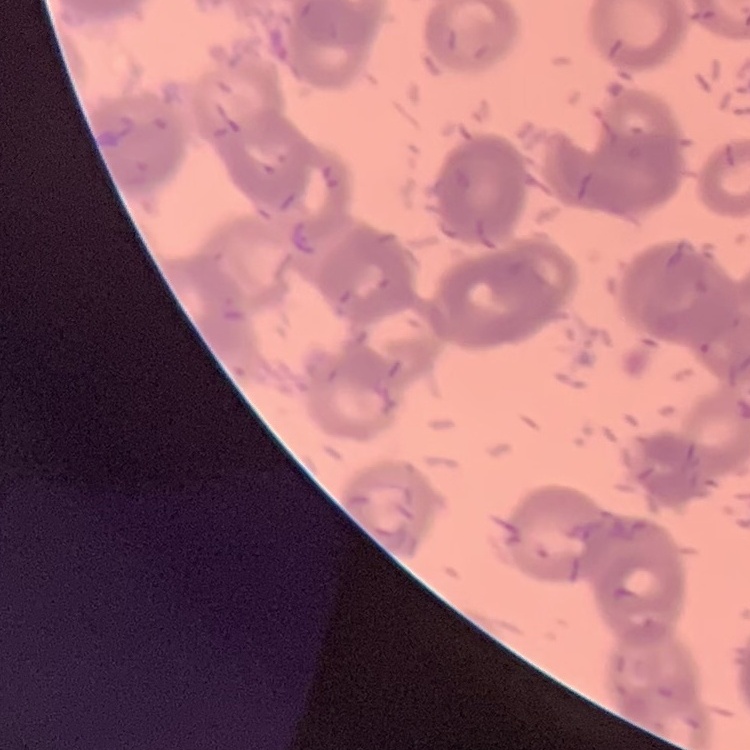 The red blood cells exhibit rouleaux formation. One tile cut from a larger photomicrograph. Stained with either Field's or Giemsa. Thin blood smear.